Assess this cell for malaria.
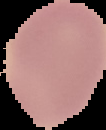

It is uninfected.

The area outside the segmented cell region is set to black. Image is 106×130 pixels. From a thin blood film.